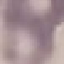 Malaria status: uninfected. Giemsa-stained preparation. Photographed with a smartphone camera at the microscope eyepiece. Thin smear of blood. Automatically extracted cell patch, resized to 64 × 64 pixels.